Outline each blood parasite and name the species.
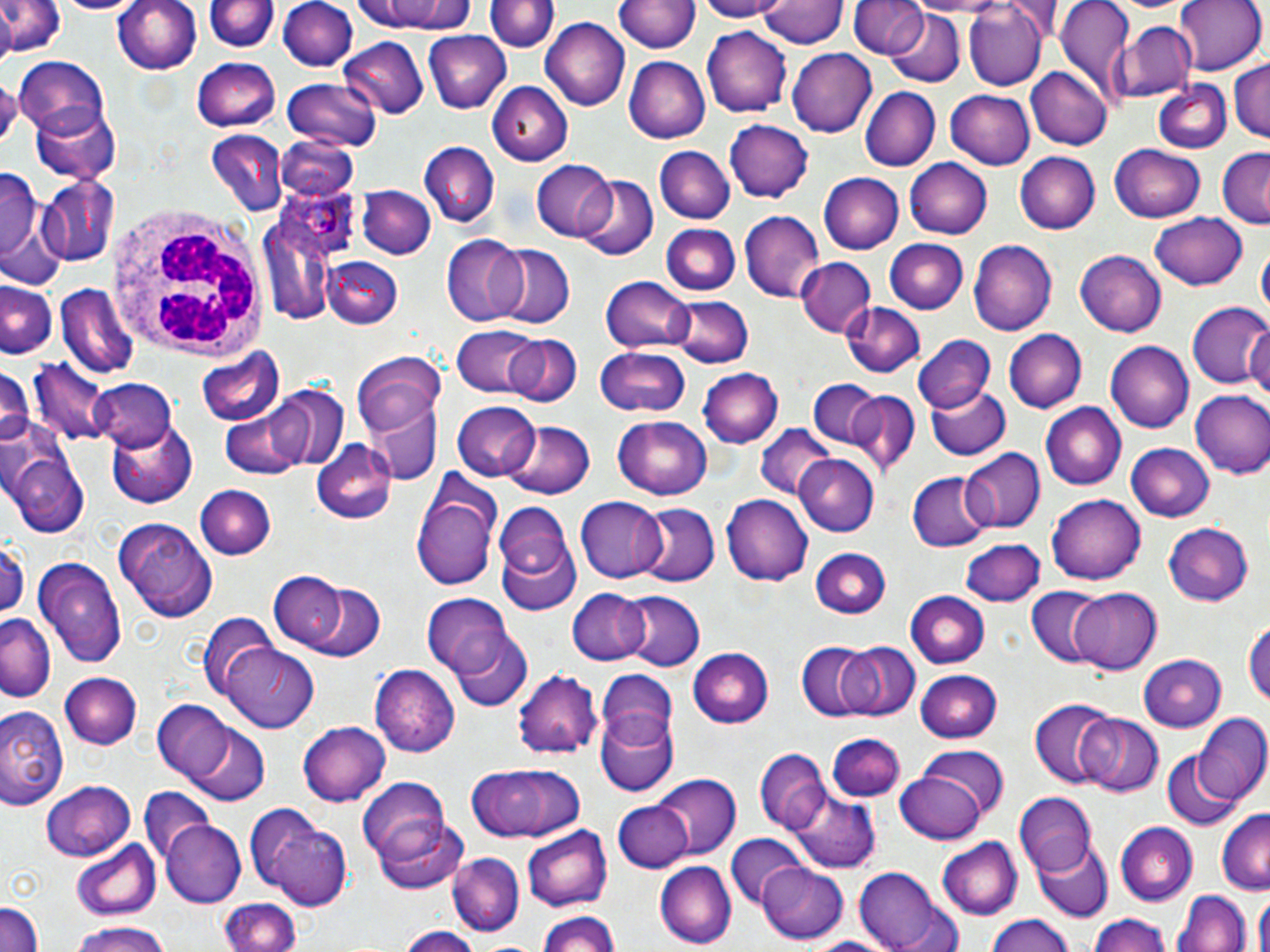

Approximate bounding boxes as named x1/y1/x2/y2 corners in pixels.
Plasmodium ovale-infected red blood cells: (x1=277, y1=181, x2=359, y2=260).
No Plasmodium falciparum, Plasmodium malariae, Plasmodium vivax, Babesia divergens, or Trypanosoma brucei observed.

slide-level diagnosis = Plasmodium ovale
field of view = one of a larger specimen
preparation = thin blood smear
modality = light microscopy
uninfected red blood cell locations = approximate bounding boxes as named x1/y1/x2/y2 corners in pixels: (x1=0, y1=0, x2=65, y2=58), (x1=50, y1=0, x2=147, y2=16), (x1=111, y1=0, x2=203, y2=77), (x1=280, y1=0, x2=356, y2=71), (x1=488, y1=0, x2=555, y2=55), (x1=691, y1=0, x2=790, y2=21), (x1=760, y1=0, x2=845, y2=50), (x1=851, y1=0, x2=927, y2=58), (x1=1053, y1=0, x2=1135, y2=100), (x1=1175, y1=0, x2=1265, y2=76), (x1=207, y1=1, x2=275, y2=54), (x1=354, y1=1, x2=478, y2=35), (x1=615, y1=1, x2=700, y2=56), (x1=1109, y1=1, x2=1195, y2=15), (x1=964, y1=2, x2=1048, y2=90), (x1=885, y1=9, x2=964, y2=86), (x1=541, y1=19, x2=629, y2=110), (x1=1117, y1=23, x2=1198, y2=103), (x1=704, y1=26, x2=793, y2=117), (x1=422, y1=31, x2=511, y2=113), (x1=340, y1=37, x2=430, y2=118), (x1=787, y1=47, x2=877, y2=137), (x1=625, y1=55, x2=711, y2=144), (x1=13, y1=56, x2=109, y2=142), (x1=1228, y1=58, x2=1270, y2=143), (x1=193, y1=59, x2=281, y2=129), (x1=1027, y1=66, x2=1113, y2=151), (x1=1187, y1=67, x2=1270, y2=146), (x1=283, y1=77, x2=383, y2=154), (x1=1151, y1=81, x2=1231, y2=154), (x1=486, y1=82, x2=572, y2=164), (x1=860, y1=87, x2=941, y2=171), (x1=946, y1=89, x2=1035, y2=170), (x1=28, y1=99, x2=120, y2=183), (x1=725, y1=120, x2=813, y2=203), (x1=207, y1=130, x2=288, y2=213), (x1=655, y1=133, x2=812, y2=214), (x1=275, y1=136, x2=360, y2=201), (x1=419, y1=141, x2=498, y2=225), (x1=1111, y1=142, x2=1208, y2=223), (x1=655, y1=145, x2=733, y2=224), (x1=1216, y1=148, x2=1270, y2=228), (x1=1015, y1=152, x2=1099, y2=234), (x1=903, y1=157, x2=993, y2=241), (x1=533, y1=162, x2=618, y2=240), (x1=0, y1=169, x2=42, y2=263), (x1=819, y1=172, x2=904, y2=253), (x1=571, y1=175, x2=659, y2=261), (x1=38, y1=176, x2=117, y2=266), (x1=358, y1=186, x2=436, y2=260), (x1=258, y1=206, x2=342, y2=326), (x1=738, y1=209, x2=825, y2=301), (x1=1149, y1=211, x2=1248, y2=290), (x1=662, y1=223, x2=740, y2=296), (x1=440, y1=236, x2=529, y2=326), (x1=967, y1=238, x2=1059, y2=336), (x1=884, y1=239, x2=969, y2=313), (x1=492, y1=245, x2=574, y2=330), (x1=1257, y1=246, x2=1269, y2=321), (x1=1074, y1=250, x2=1167, y2=336), (x1=321, y1=258, x2=401, y2=328), (x1=795, y1=259, x2=875, y2=338), (x1=601, y1=276, x2=694, y2=354), (x1=2, y1=279, x2=59, y2=359), (x1=56, y1=284, x2=136, y2=378), (x1=667, y1=294, x2=754, y2=367), (x1=839, y1=300, x2=925, y2=379), (x1=1186, y1=302, x2=1270, y2=390), (x1=1244, y1=319, x2=1270, y2=404), (x1=452, y1=325, x2=544, y2=397), (x1=1004, y1=329, x2=1087, y2=415), (x1=503, y1=333, x2=581, y2=408), (x1=915, y1=337, x2=995, y2=416), (x1=1106, y1=340, x2=1194, y2=433), (x1=595, y1=346, x2=692, y2=417), (x1=196, y1=348, x2=285, y2=430), (x1=351, y1=353, x2=448, y2=434), (x1=30, y1=358, x2=115, y2=448), (x1=0, y1=361, x2=35, y2=453), (x1=696, y1=367, x2=780, y2=448), (x1=807, y1=378, x2=883, y2=451), (x1=89, y1=379, x2=177, y2=451), (x1=926, y1=382, x2=1010, y2=460), (x1=267, y1=384, x2=350, y2=471), (x1=220, y1=390, x2=326, y2=477), (x1=1188, y1=390, x2=1270, y2=480), (x1=844, y1=392, x2=920, y2=477), (x1=453, y1=401, x2=539, y2=478), (x1=365, y1=402, x2=440, y2=482), (x1=1042, y1=403, x2=1126, y2=490), (x1=612, y1=415, x2=712, y2=499), (x1=105, y1=420, x2=196, y2=508), (x1=503, y1=421, x2=594, y2=500), (x1=753, y1=424, x2=835, y2=501), (x1=0, y1=426, x2=89, y2=541), (x1=311, y1=441, x2=398, y2=526), (x1=1127, y1=443, x2=1217, y2=522), (x1=962, y1=447, x2=1044, y2=533), (x1=792, y1=455, x2=876, y2=536), (x1=907, y1=472, x2=989, y2=552), (x1=412, y1=479, x2=499, y2=593), (x1=194, y1=485, x2=274, y2=561), (x1=721, y1=494, x2=814, y2=585), (x1=1047, y1=495, x2=1146, y2=586), (x1=576, y1=497, x2=669, y2=584), (x1=494, y1=500, x2=580, y2=611), (x1=634, y1=503, x2=718, y2=588), (x1=115, y1=518, x2=217, y2=621), (x1=1162, y1=522, x2=1252, y2=606), (x1=961, y1=538, x2=1044, y2=607), (x1=0, y1=542, x2=27, y2=619), (x1=808, y1=547, x2=892, y2=619), (x1=35, y1=556, x2=126, y2=669), (x1=268, y1=571, x2=347, y2=649), (x1=303, y1=583, x2=385, y2=661), (x1=1027, y1=586, x2=1107, y2=667), (x1=1069, y1=587, x2=1163, y2=674), (x1=566, y1=589, x2=652, y2=665), (x1=906, y1=589, x2=988, y2=668), (x1=617, y1=590, x2=704, y2=673), (x1=423, y1=593, x2=516, y2=681), (x1=1242, y1=612, x2=1270, y2=716), (x1=202, y1=614, x2=281, y2=702), (x1=0, y1=616, x2=54, y2=700), (x1=451, y1=632, x2=531, y2=711), (x1=795, y1=639, x2=877, y2=723), (x1=837, y1=640, x2=920, y2=722), (x1=688, y1=645, x2=773, y2=726), (x1=224, y1=646, x2=319, y2=734), (x1=1138, y1=650, x2=1226, y2=728), (x1=372, y1=665, x2=459, y2=756), (x1=597, y1=669, x2=675, y2=745), (x1=916, y1=669, x2=1003, y2=742), (x1=60, y1=671, x2=142, y2=749), (x1=514, y1=671, x2=604, y2=761), (x1=1029, y1=700, x2=1116, y2=789), (x1=151, y1=702, x2=241, y2=786), (x1=0, y1=707, x2=66, y2=804), (x1=171, y1=711, x2=274, y2=803), (x1=596, y1=711, x2=677, y2=797), (x1=1074, y1=713, x2=1163, y2=796), (x1=1193, y1=714, x2=1270, y2=806), (x1=299, y1=721, x2=390, y2=806), (x1=828, y1=732, x2=905, y2=802), (x1=916, y1=745, x2=1008, y2=827), (x1=755, y1=747, x2=830, y2=834), (x1=1158, y1=749, x2=1244, y2=832), (x1=467, y1=760, x2=586, y2=845), (x1=897, y1=767, x2=992, y2=843), (x1=650, y1=775, x2=741, y2=860), (x1=358, y1=778, x2=450, y2=864), (x1=39, y1=779, x2=133, y2=861), (x1=140, y1=787, x2=213, y2=867), (x1=1014, y1=791, x2=1096, y2=874), (x1=788, y1=792, x2=879, y2=873), (x1=244, y1=800, x2=357, y2=912), (x1=614, y1=801, x2=693, y2=873), (x1=1215, y1=809, x2=1270, y2=893), (x1=371, y1=814, x2=468, y2=895), (x1=160, y1=819, x2=244, y2=908), (x1=1113, y1=822, x2=1196, y2=907), (x1=521, y1=826, x2=612, y2=912), (x1=723, y1=832, x2=805, y2=910), (x1=936, y1=836, x2=1024, y2=919), (x1=71, y1=838, x2=159, y2=921), (x1=1031, y1=841, x2=1113, y2=922), (x1=448, y1=853, x2=523, y2=937), (x1=756, y1=861, x2=849, y2=943), (x1=655, y1=862, x2=735, y2=947), (x1=853, y1=867, x2=957, y2=952), (x1=1174, y1=890, x2=1252, y2=952), (x1=1253, y1=896, x2=1270, y2=952), (x1=218, y1=898, x2=302, y2=952), (x1=0, y1=899, x2=43, y2=952), (x1=534, y1=908, x2=624, y2=952), (x1=1086, y1=914, x2=1173, y2=952), (x1=984, y1=915, x2=1076, y2=952), (x1=68, y1=920, x2=173, y2=952), (x1=394, y1=926, x2=483, y2=952), (x1=804, y1=935, x2=898, y2=952)
magnification = 1000x
stain = May-Grünwald-Giemsa
white blood cell locations = approximate bounding boxes as named x1/y1/x2/y2 corners in pixels: (x1=107, y1=203, x2=275, y2=365)
image size = 1270×952 pixels